Comment on the morphology of the erythrocytes.
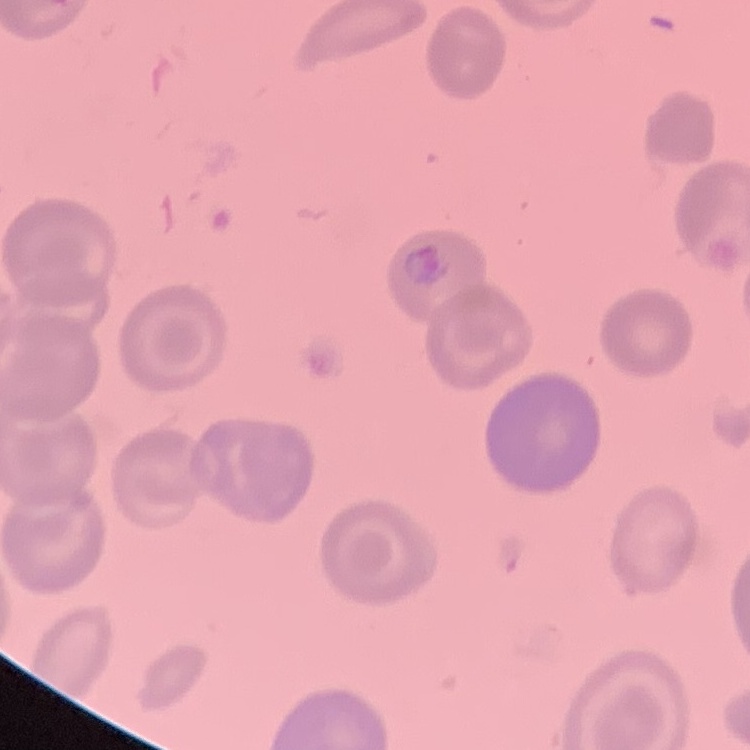

They show no rouleaux formation.

image type = square crop of a larger photomicrograph
stain = Field's or Giemsa
preparation = thin blood film